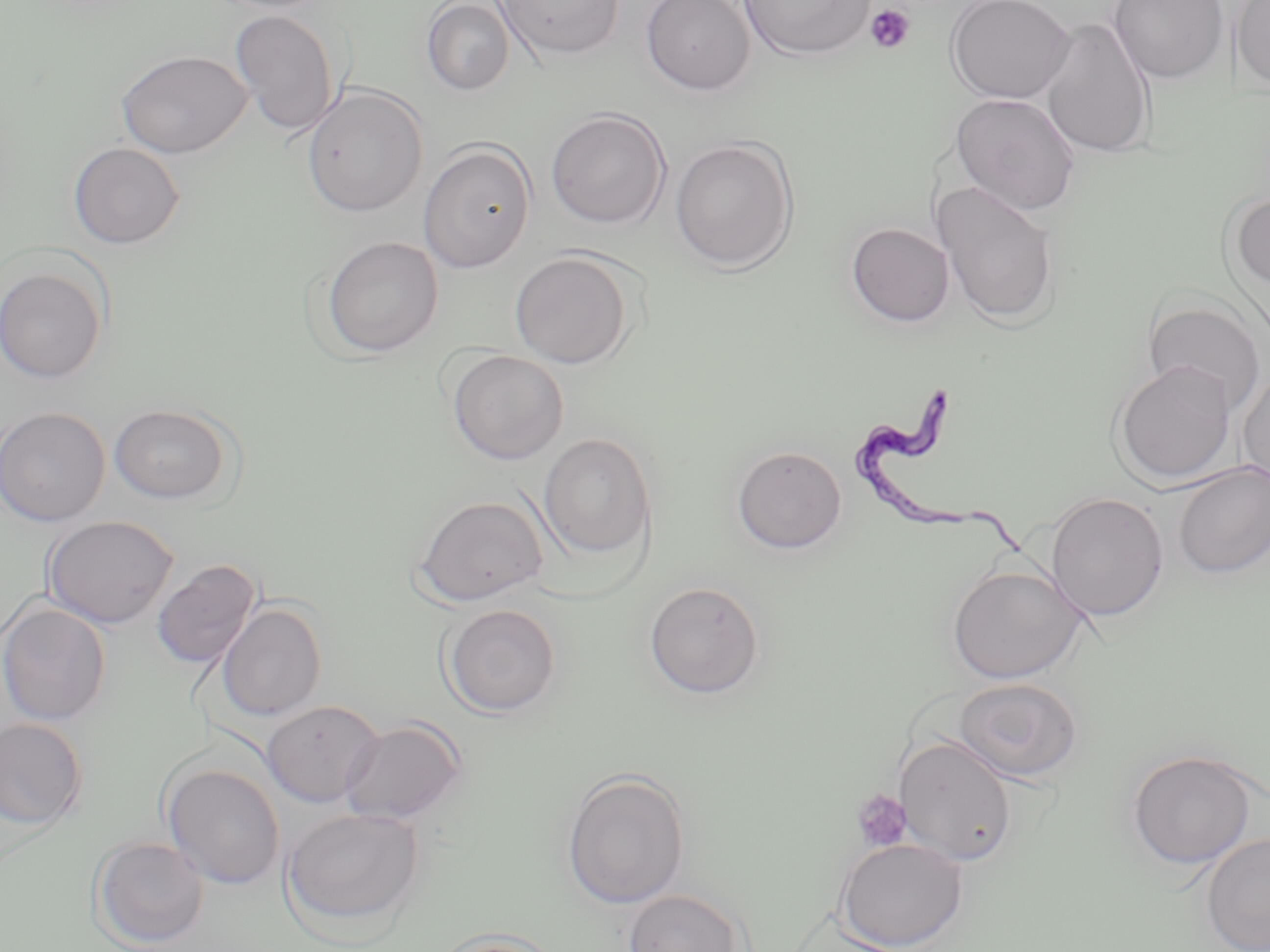 Approximate bounding boxes as (x1, y1, x2, y2) in pixels. Platelet locations: (864, 4, 916, 54), (851, 789, 912, 852). Trypanosoma brucei locations: (850, 385, 1039, 571). Uninfected red blood cell locations: (421, 0, 515, 96), (492, 0, 626, 61), (641, 0, 756, 95), (738, 0, 876, 61), (945, 0, 1076, 104), (1107, 0, 1229, 84), (1230, 0, 1270, 92), (229, 9, 341, 137), (1038, 16, 1156, 160), (116, 49, 253, 158), (301, 85, 429, 218), (950, 93, 1081, 216), (545, 108, 671, 230), (669, 137, 799, 272), (418, 141, 536, 273), (67, 142, 185, 249), (933, 180, 1060, 327), (1227, 191, 1270, 294), (845, 221, 954, 328), (320, 236, 444, 358), (509, 251, 635, 369), (0, 264, 110, 385), (1142, 296, 1266, 413), (447, 350, 569, 465), (1112, 360, 1237, 485), (1237, 369, 1270, 489), (110, 402, 235, 505), (0, 406, 110, 527), (539, 432, 657, 562), (731, 444, 847, 554), (1171, 462, 1270, 579), (1044, 491, 1169, 622), (413, 494, 550, 607), (430, 496, 554, 720), (41, 515, 179, 629), (151, 558, 261, 670), (946, 563, 1086, 683), (643, 580, 765, 700), (0, 600, 111, 726), (216, 602, 327, 722), (442, 603, 562, 718), (954, 677, 1083, 783), (261, 699, 385, 808), (0, 718, 89, 830), (339, 718, 468, 826), (893, 734, 1017, 867), (1125, 748, 1261, 869), (161, 762, 286, 890), (560, 769, 691, 910), (282, 806, 425, 933), (1201, 832, 1270, 952), (91, 836, 210, 949), (835, 837, 969, 950), (623, 888, 745, 952), (431, 931, 566, 952). Slide-level diagnosis: Trypanosoma brucei. Thin blood smear. Image is 1270×952 pixels. Optical microscopy. May-Grünwald-Giemsa-stained preparation. Captured at 1000x magnification. One field of a larger specimen.